Name the parasite shown.
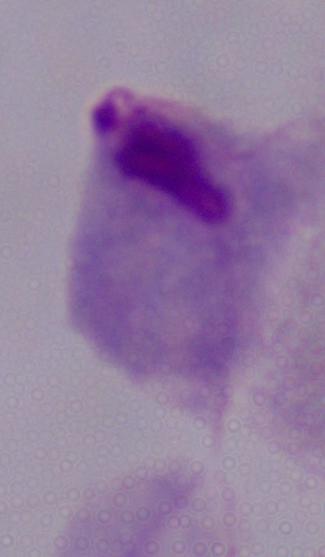

This is a trichomonad.

modality = micrograph
magnification = 1000x